Identify the preparation type.
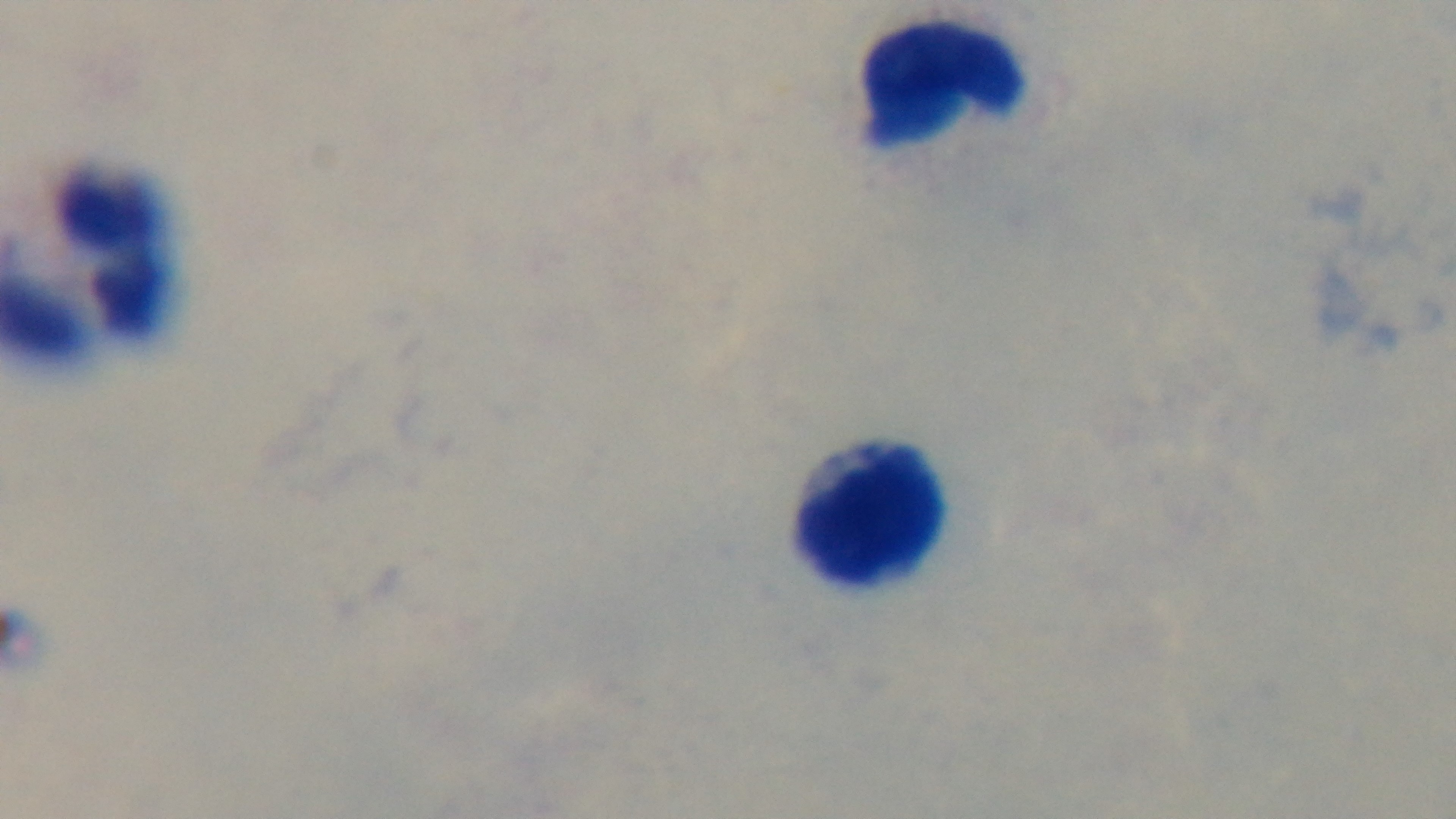
Thick.

{
  "objective": "100x oil immersion",
  "field_of_view": "single",
  "stain": "Giemsa",
  "modality": "light microscopy",
  "capture": "mounted 4K digital camera",
  "malaria_status": "uninfected"
}